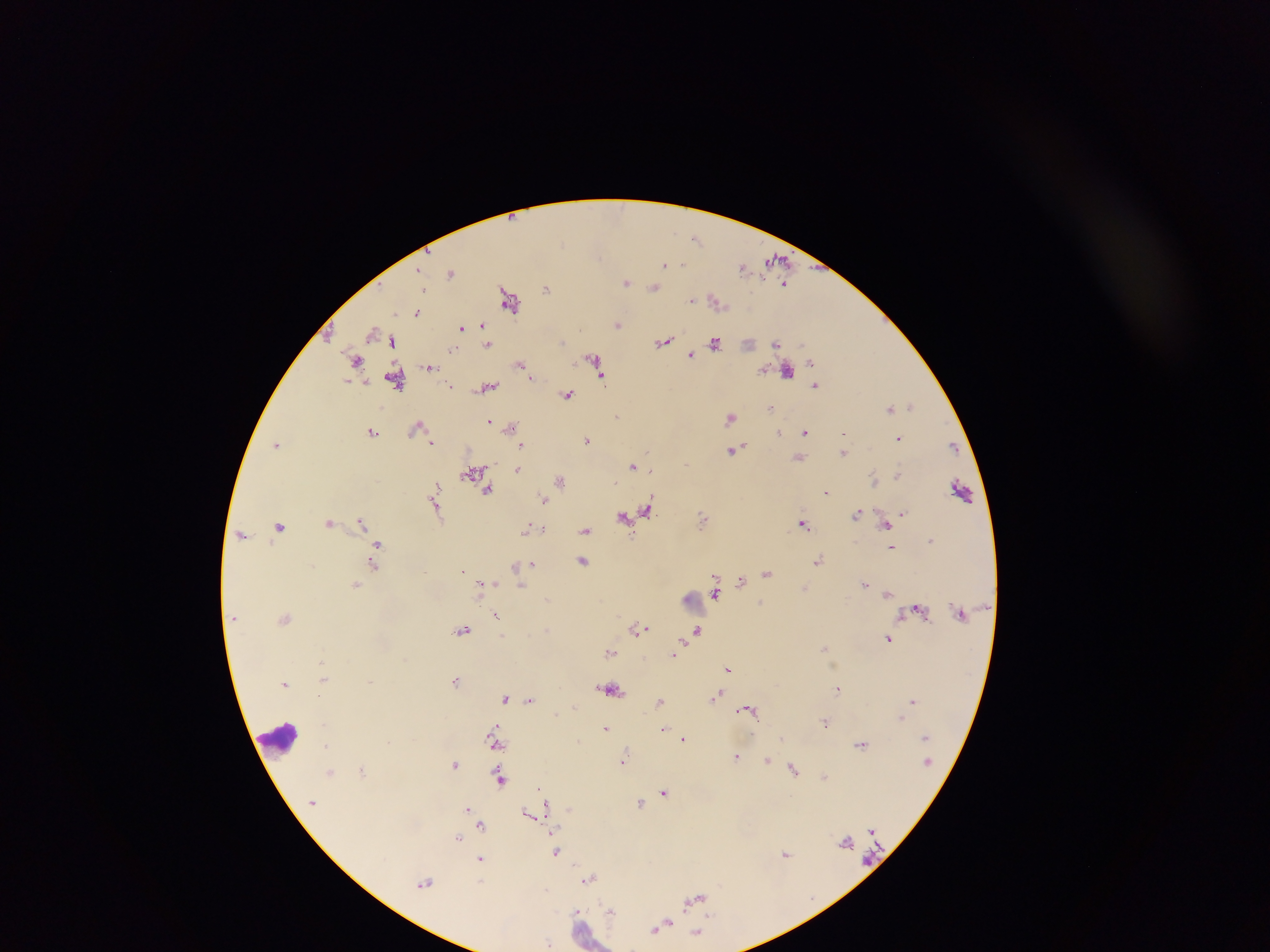
Approximate centers as x y in pixels.
Summary:
  - Plasmodium parasite locations (subset; some below the resolvable size): 697 237; 664 264; 683 264; 743 266; 424 290; 547 290; 691 300; 418 312; 482 324; 463 328; 368 342; 776 342; 457 346; 487 346; 450 352; 692 354; 522 368; 816 385; 451 388; 568 394; 771 408; 617 417; 488 421; 780 431; 372 433; 805 433; 900 438; 588 440; 432 441; 521 447; 847 452; 731 453; 686 464; 631 466; 652 468; 518 470; 897 474; 828 493; 545 499; 903 511; 858 514; 703 516; 361 519; 803 523; 885 526; 280 527; 527 529; 587 530; 243 537; 272 543; 378 543; 929 543; 892 548; 818 558; 534 563; 371 565; 767 574; 716 577; 741 580; 483 582; 864 582; 355 585; 887 594; 915 608; 497 614; 464 628; 640 628; 697 630; 503 636; 888 639; 825 647; 610 653; 671 656; 728 671; 456 680; 286 685; 837 689; 719 696; 504 698; 530 701; 660 701; 913 701; 744 708; 759 722; 825 722; 494 727; 607 728; 663 729; 686 739; 780 739; 861 742; 496 747; 736 757; 767 760; 624 763; 455 764; 499 767; 360 769; 796 770; 825 776; 501 780; 537 786; 663 790; 640 802; 545 805; 466 808; 570 808; 528 813; 482 823; 869 831; 459 837; 846 840; 557 851; 786 853; 479 861; 589 878; 480 881; 426 882; 575 909; 710 914; 669 924
  - Leukocyte locations: 282 734
  - Capture: mobile-phone photograph through a microscope
  - Field of view: single
  - Country: Ghana
  - Image size: 1270×952 pixels
  - Preparation: thick blood film